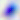

{
  "identification": "Toxoplasma gondii",
  "modality": "photomicrograph",
  "magnification": "400x"
}